Locate every blood parasite and identify its species.
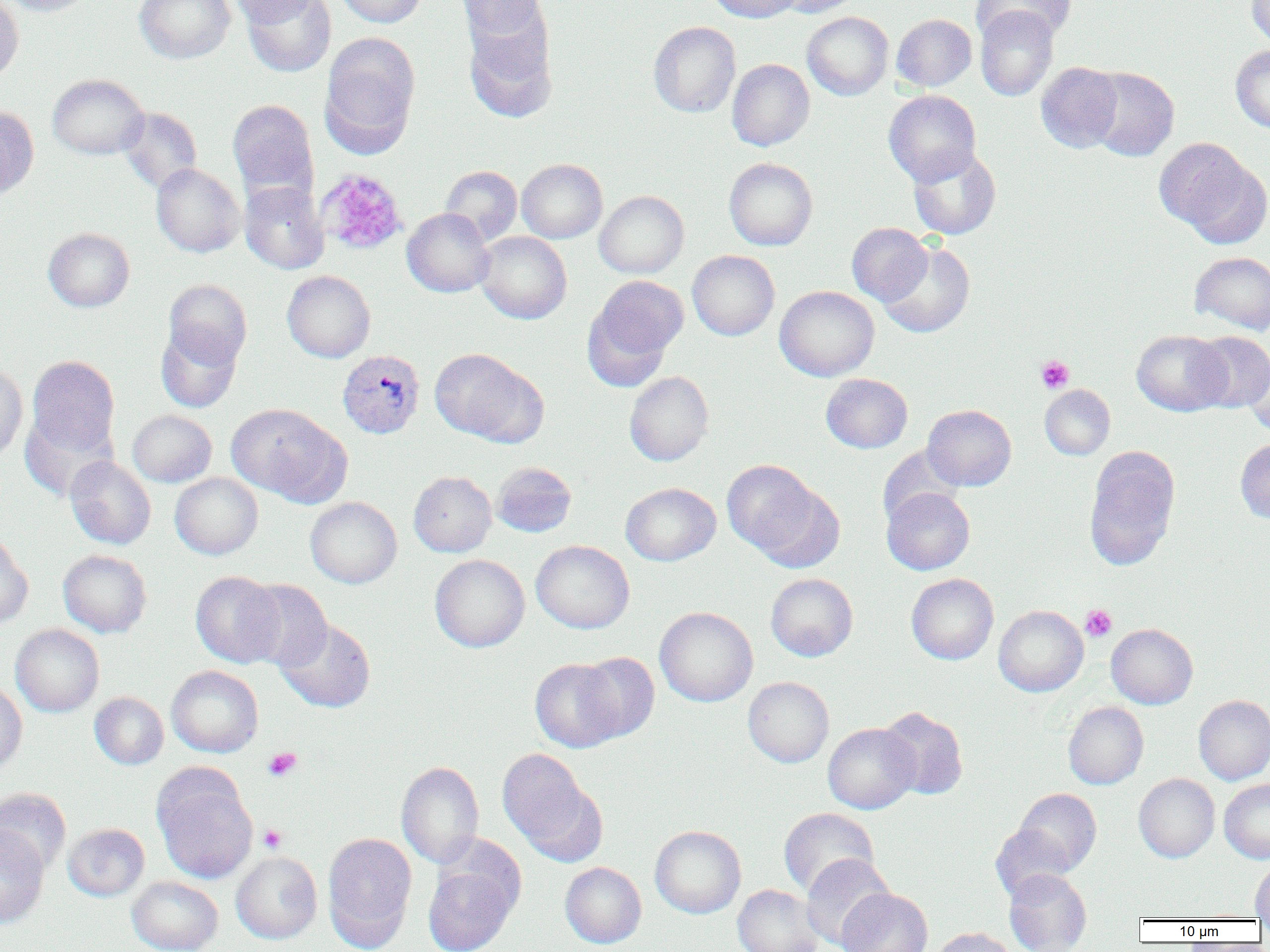
Approximate bounding boxes as (x1,y1)-(x2,y2) corner pairs in pixels.
Plasmodium vivax-infected red blood cells: (337,350)-(425,439).
No Plasmodium falciparum, Plasmodium ovale, Plasmodium malariae, Babesia divergens, or Trypanosoma brucei observed.

slide-level diagnosis = Plasmodium vivax
modality = light microscopy
platelet locations (subset) = approximate bounding boxes as (x1,y1)-(x2,y2) corner pairs in pixels: (1036,355)-(1075,393), (1080,605)-(1116,641), (263,747)-(302,781), (259,825)-(287,852)
uninfected red blood cell locations (subset) = approximate bounding boxes as (x1,y1)-(x2,y2) corner pairs in pixels: (0,0)-(96,16), (0,0)-(23,84), (134,0)-(235,64), (228,0)-(320,25), (241,0)-(336,77), (334,0)-(426,27), (456,0)-(547,42), (706,0)-(803,23), (773,0)-(862,17), (971,0)-(1075,44), (1246,1)-(1270,49), (975,5)-(1059,101), (463,9)-(558,122), (802,12)-(893,100), (892,14)-(976,91), (648,21)-(740,117), (319,34)-(420,155), (1231,45)-(1270,133), (727,59)-(815,151), (1036,62)-(1123,152), (1086,66)-(1179,161), (47,74)-(149,159), (884,90)-(981,186), (227,99)-(318,202), (0,105)-(38,199), (119,107)-(201,194), (1156,139)-(1266,244), (908,146)-(1001,240), (724,157)-(818,250), (517,159)-(607,243), (151,163)-(244,257), (440,166)-(522,245), (240,181)-(329,274), (594,190)-(689,278), (402,208)-(495,297), (847,222)-(932,305), (43,228)-(135,312), (475,231)-(572,324), (878,241)-(976,338), (687,250)-(780,341), (1189,251)-(1270,334), (282,270)-(375,362), (585,276)-(687,385), (163,279)-(252,368), (774,285)-(879,381), (156,324)-(242,413), (1132,330)-(1230,416), (1190,332)-(1270,411), (429,347)-(546,446), (27,355)-(120,458), (1243,355)-(1270,435), (0,364)-(28,463), (624,371)-(714,466), (821,373)-(913,453), (1040,385)-(1115,460), (227,403)-(349,505), (923,405)-(1016,491), (128,410)-(217,487), (19,411)-(116,501), (1235,438)-(1270,524), (877,446)-(964,528), (1084,446)-(1180,570), (65,456)-(156,549), (722,460)-(833,566), (492,462)-(576,537), (409,471)-(497,557), (170,473)-(263,559), (620,482)-(721,566), (882,487)-(975,575), (305,497)-(402,588), (0,531)-(33,630), (531,540)-(634,633), (58,549)-(152,637), (430,554)-(529,652), (190,570)-(285,668), (766,573)-(858,661), (906,573)-(999,664), (241,580)-(332,671), (993,605)-(1088,696), (654,606)-(758,707), (276,618)-(376,712), (1106,623)-(1198,709), (10,624)-(104,717), (575,652)-(660,743), (529,658)-(627,753), (166,665)-(264,757), (743,676)-(834,767), (0,680)-(27,775), (89,692)-(168,769), (1193,695)-(1270,785), (1063,701)-(1148,789), (878,706)-(968,800), (822,722)-(919,814), (496,748)-(603,862), (396,761)-(484,869), (152,766)-(258,884), (1134,773)-(1220,863), (1220,780)-(1270,863), (0,787)-(71,875), (1012,788)-(1102,876), (778,807)-(879,898), (63,823)-(149,901), (990,823)-(1078,900), (0,824)-(49,929), (649,825)-(746,918), (322,832)-(417,950), (231,851)-(322,943), (801,854)-(894,948), (423,859)-(519,952), (1250,860)-(1270,919), (560,862)-(646,948), (1004,869)-(1092,952), (127,876)-(223,952), (732,885)-(824,952), (836,888)-(933,952), (928,927)-(1017,952)
preparation = thin blood smear
magnification = 1000x
image size = 1270×952 pixels
field of view = single